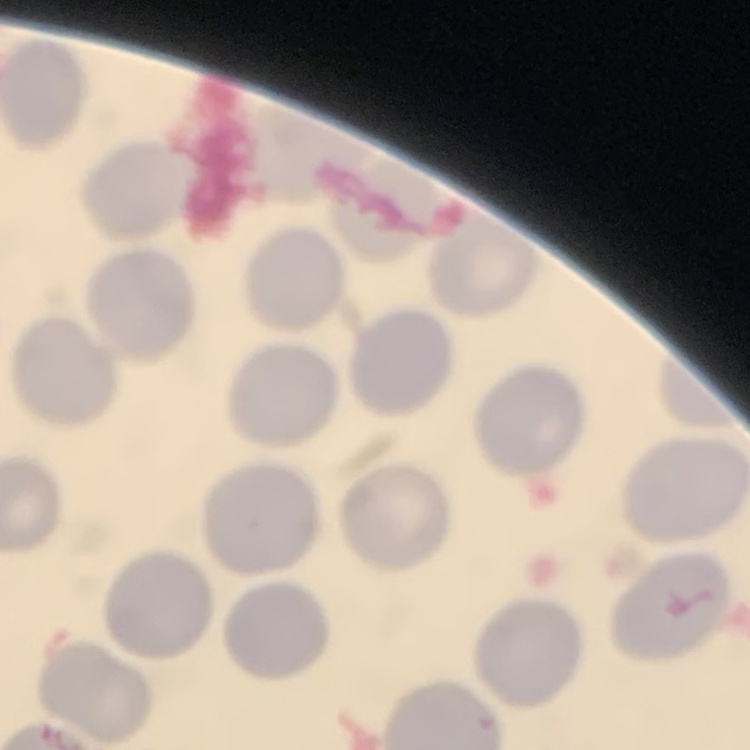
Summary:
  - Red blood cell morphology: no rouleaux formation
  - Image type: square crop of a larger photomicrograph
  - Preparation: thin blood film
  - Stain: Field's or Giemsa